Locate every blood parasite and identify its species.
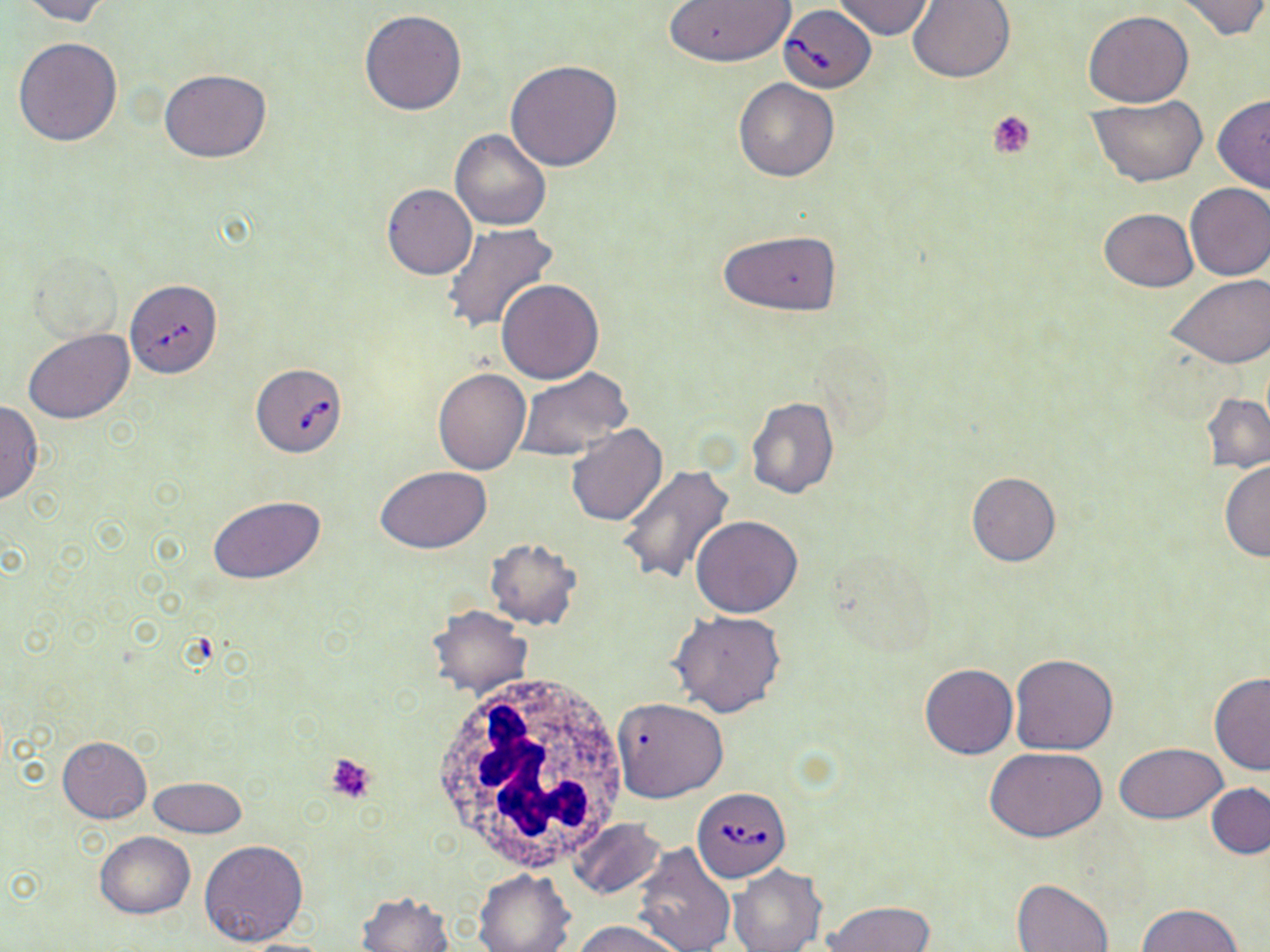

Approximate bounding boxes as (x1, y1, x2, y2) in pixels.
Babesia divergens-infected red blood cells: (778, 6, 876, 92), (124, 285, 229, 385), (252, 362, 348, 457), (693, 786, 790, 882).
No Plasmodium falciparum, Plasmodium ovale, Plasmodium malariae, Plasmodium vivax, or Trypanosoma brucei observed.

slide-level diagnosis = Babesia divergens
stain = May-Grünwald-Giemsa
white blood cell locations = approximate bounding boxes as (x1, y1, x2, y2) in pixels: (427, 672, 628, 871)
uninfected red blood cell locations = approximate bounding boxes as (x1, y1, x2, y2) in pixels: (12, 0, 110, 24), (834, 0, 934, 40), (1170, 0, 1269, 40), (661, 1, 797, 68), (908, 1, 1015, 83), (359, 8, 466, 115), (1083, 11, 1193, 107), (12, 37, 123, 146), (505, 60, 623, 171), (160, 69, 272, 162), (734, 78, 839, 183), (1212, 95, 1270, 193), (1089, 96, 1210, 185), (451, 129, 552, 231), (1184, 182, 1270, 279), (382, 184, 476, 281), (1099, 208, 1198, 291), (441, 222, 559, 335), (719, 229, 841, 317), (29, 247, 125, 347), (1167, 275, 1270, 369), (496, 278, 603, 383), (23, 329, 134, 424), (432, 366, 530, 473), (513, 368, 635, 463), (1201, 393, 1270, 474), (745, 396, 839, 499), (0, 400, 44, 503), (566, 425, 667, 528), (1219, 460, 1270, 562), (375, 466, 491, 553), (618, 466, 735, 588), (966, 471, 1061, 567), (207, 495, 326, 584), (691, 516, 803, 618), (485, 537, 582, 630), (822, 553, 937, 658), (427, 604, 532, 698), (668, 610, 786, 717), (1009, 652, 1120, 755), (920, 663, 1017, 758), (1209, 673, 1270, 774), (613, 697, 729, 803), (57, 735, 151, 822), (1114, 742, 1227, 823), (986, 747, 1107, 842), (148, 776, 247, 837), (1206, 783, 1270, 859), (568, 818, 666, 898), (94, 832, 195, 919), (199, 840, 310, 948), (632, 841, 737, 952), (728, 865, 826, 952), (474, 868, 574, 952), (1011, 879, 1115, 951), (358, 890, 454, 951), (823, 900, 933, 952), (1136, 904, 1245, 952), (571, 920, 681, 952)
platelet locations = approximate bounding boxes as (x1, y1, x2, y2) in pixels: (987, 110, 1037, 160), (324, 752, 378, 806)
image size = 1270×952 pixels
preparation = thin blood film
field of view = one of a larger specimen
modality = light microscopy
magnification = 1000x